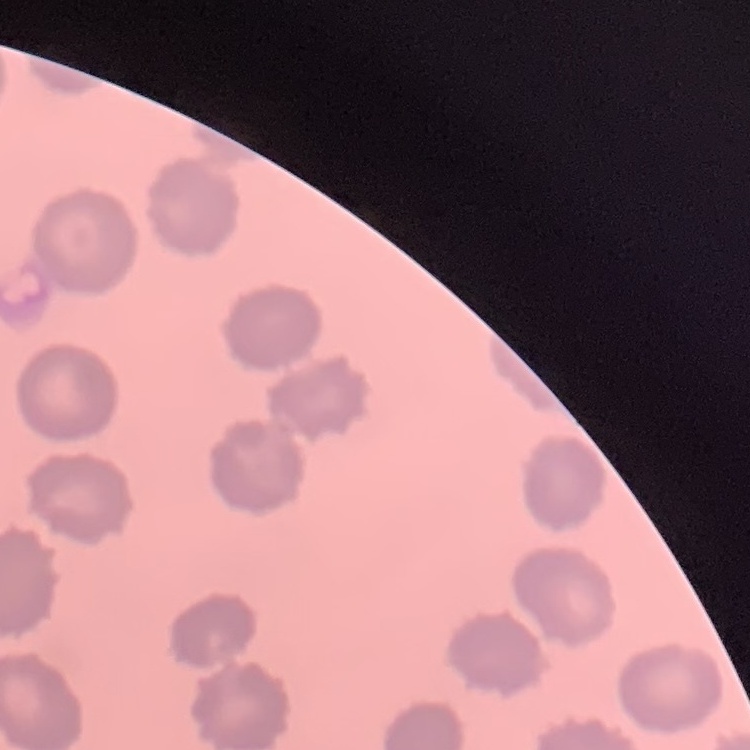 The red blood cells show no rouleaux formation. One tile cut from a larger photomicrograph. Thin blood smear. Stained with either Field's or Giemsa.